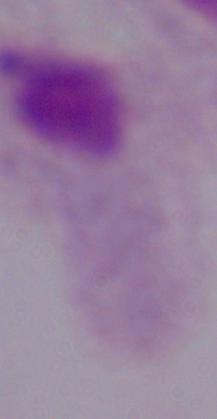
Summary:
  - Magnification: 1000x
  - Identification: trichomonad
  - Modality: photomicrograph